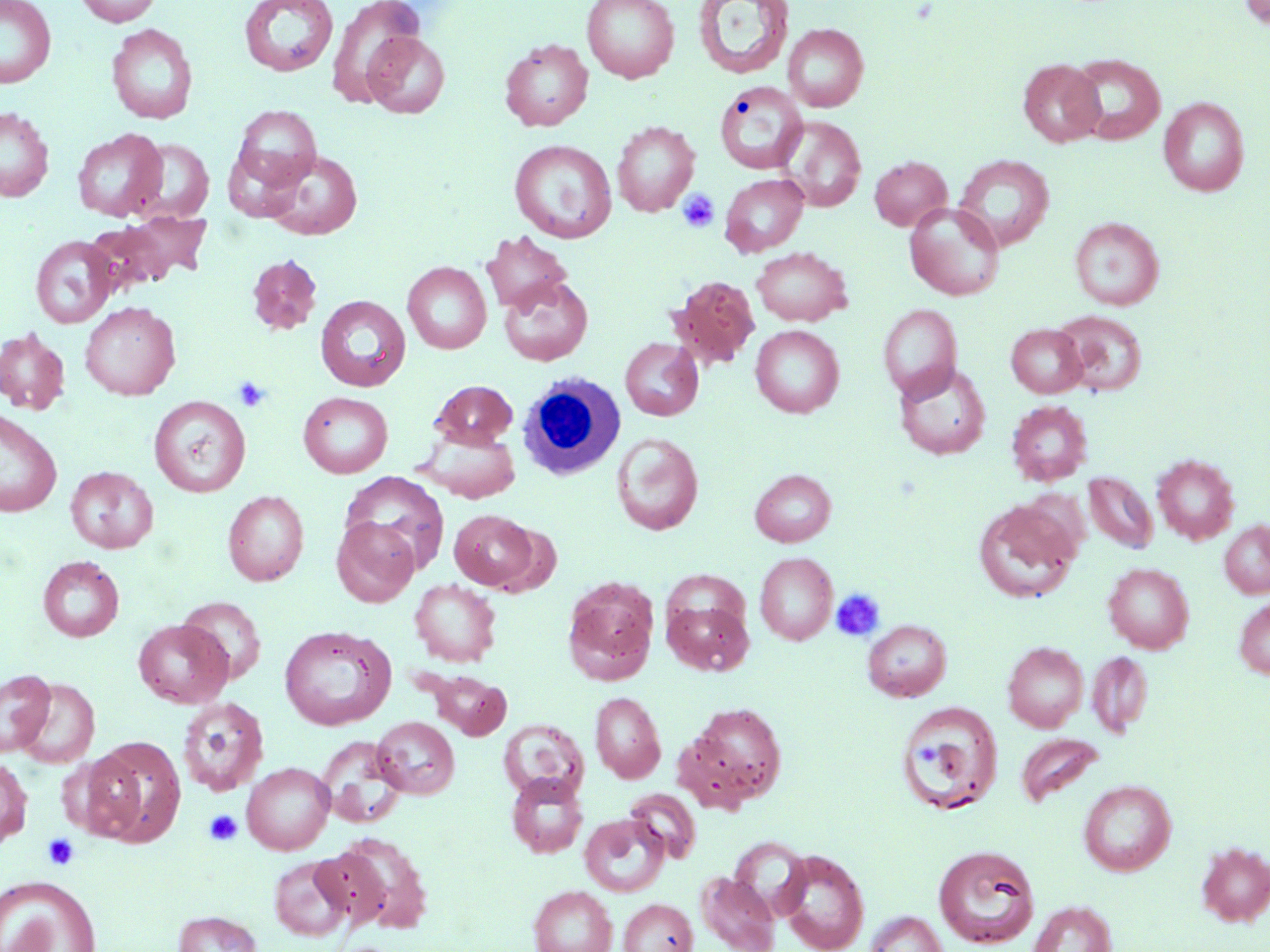

{
  "slide_level_diagnosis": "negative for blood parasites",
  "white_blood_cell_locations": "approximate bounding boxes as (x1,y1)-(x2,y2) corner pairs in pixels: (517,373)-(625,480)",
  "field_of_view": "one of a larger specimen",
  "modality": "light microscopy",
  "stain": "May-Grünwald-Giemsa",
  "platelet_locations": "approximate bounding boxes as (x1,y1)-(x2,y2) corner pairs in pixels: (677,188)-(720,233), (233,376)-(271,413), (830,588)-(886,641), (204,809)-(243,846), (43,833)-(79,870)",
  "image_size": "1270×952 pixels",
  "uninfected_red_blood_cell_locations": "approximate bounding boxes as (x1,y1)-(x2,y2) corner pairs in pixels: (0,0)-(56,88), (75,0)-(162,26), (238,0)-(340,77), (325,0)-(426,106), (581,0)-(680,83), (1238,0)-(1270,29), (692,1)-(795,80), (783,23)-(869,112), (106,24)-(198,124), (361,32)-(450,119), (499,39)-(593,131), (1067,53)-(1166,145), (1018,58)-(1106,147), (715,81)-(808,175), (1159,97)-(1250,196), (232,104)-(321,192), (0,107)-(53,202), (778,116)-(866,212), (612,121)-(700,217), (72,129)-(167,221), (127,138)-(214,224), (509,140)-(617,243), (263,149)-(363,240), (953,154)-(1055,251), (869,156)-(952,230), (719,173)-(809,256), (904,203)-(1005,300), (87,211)-(212,294), (1070,216)-(1164,311), (481,231)-(573,314), (30,235)-(118,328), (752,247)-(852,326), (246,255)-(322,335), (403,261)-(491,353), (498,275)-(593,366), (669,275)-(760,369), (316,295)-(411,391), (80,301)-(181,401), (878,304)-(962,401), (1053,310)-(1147,395), (1006,324)-(1087,398), (750,325)-(844,417), (0,327)-(70,415), (620,338)-(703,420), (894,363)-(991,460), (429,380)-(518,448), (298,391)-(393,478), (148,396)-(251,497), (1006,400)-(1093,486), (0,409)-(62,518), (418,428)-(520,503), (611,432)-(704,536), (1152,454)-(1239,544), (66,466)-(158,553), (750,468)-(836,546), (340,471)-(450,574), (1083,471)-(1158,554), (223,490)-(309,585), (974,499)-(1081,603), (449,509)-(538,590), (331,516)-(419,606), (1220,520)-(1270,598), (755,552)-(838,645), (38,555)-(124,641), (1103,562)-(1194,653), (562,576)-(660,684), (409,579)-(501,666), (178,595)-(267,683), (662,596)-(754,675), (1234,596)-(1270,679), (133,619)-(233,708), (862,619)-(952,701), (279,625)-(395,731), (1003,641)-(1088,732), (1087,650)-(1153,736), (422,669)-(512,740), (0,670)-(56,757), (13,677)-(99,768), (590,692)-(665,782), (177,697)-(269,796), (895,700)-(1003,815), (682,703)-(787,810), (373,716)-(460,799), (499,719)-(587,800), (1016,733)-(1104,807), (84,736)-(187,847), (316,736)-(407,828), (0,757)-(33,848), (242,762)-(334,854), (506,774)-(589,858), (1079,780)-(1176,876), (625,788)-(701,862), (580,813)-(670,896), (327,832)-(434,934), (728,837)-(812,919), (1196,842)-(1270,926), (933,844)-(1041,949), (776,850)-(869,952), (270,855)-(353,941), (696,871)-(780,952), (0,875)-(102,951), (528,885)-(617,952), (619,898)-(698,952), (1028,901)-(1117,952), (173,910)-(262,952), (864,911)-(949,952)",
  "magnification": "1000x",
  "preparation": "thin blood smear"
}